Give the extent of all uninfected red blood cells.
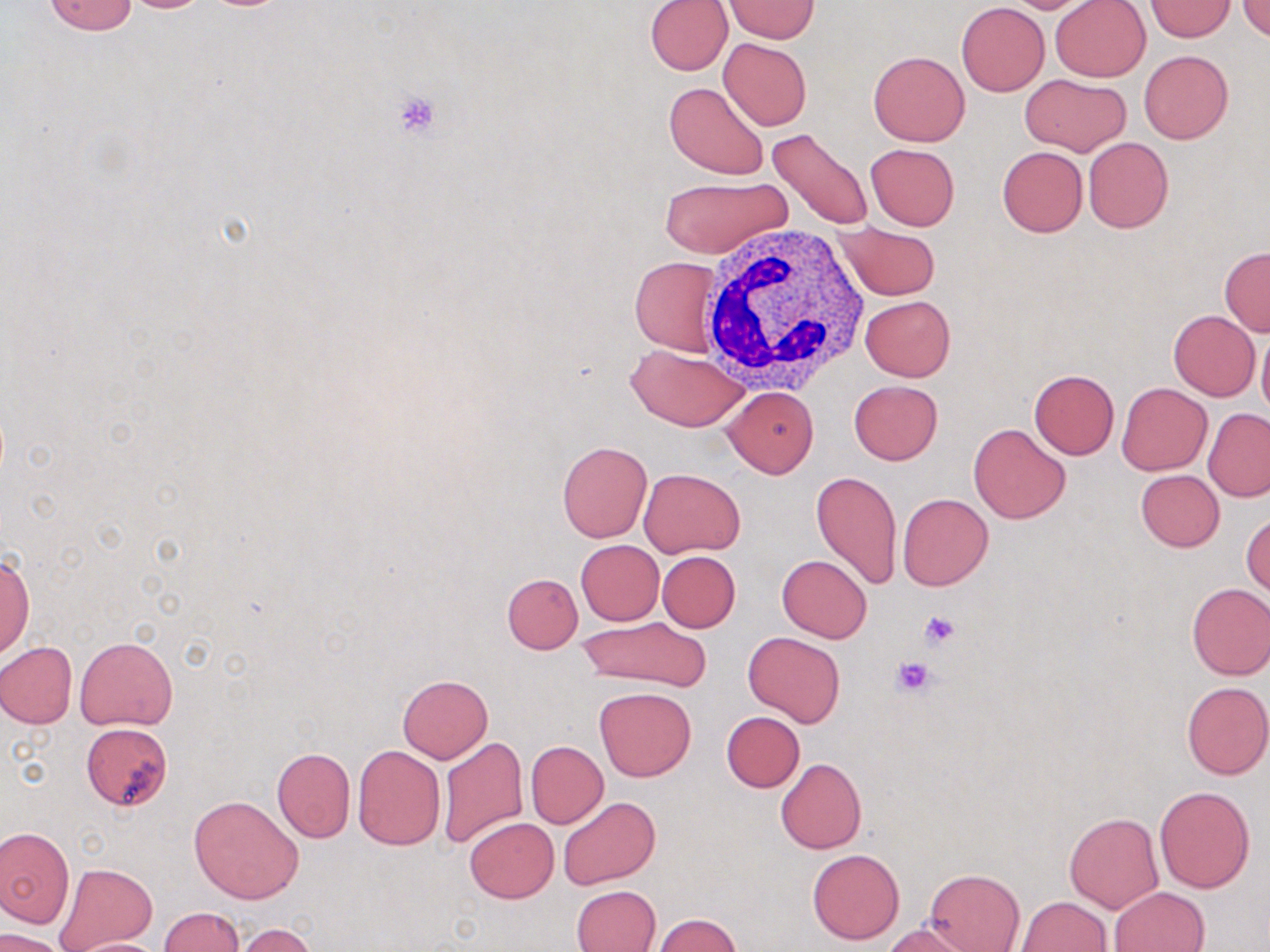

Approximate bounding boxes as [x1, y1, x2, y2] in pixels.
Uninfected red blood cells: [117, 0, 215, 13], [998, 0, 1105, 14], [1049, 0, 1150, 82], [42, 1, 140, 35], [645, 1, 732, 75], [724, 1, 819, 42], [1146, 1, 1237, 41], [1236, 1, 1270, 41], [957, 2, 1049, 96], [719, 38, 811, 130], [867, 50, 970, 146], [1140, 50, 1232, 143], [1019, 75, 1130, 156], [663, 80, 769, 179], [767, 128, 872, 231], [1083, 138, 1174, 233], [865, 143, 960, 230], [996, 146, 1088, 237], [656, 174, 792, 261], [835, 221, 941, 300], [1218, 246, 1270, 336], [629, 256, 722, 356], [860, 295, 955, 381], [1169, 310, 1259, 399], [1256, 325, 1270, 420], [627, 345, 748, 432], [1028, 369, 1120, 459], [849, 380, 943, 464], [1117, 382, 1212, 475], [722, 386, 818, 478], [1203, 408, 1270, 500], [968, 422, 1071, 524], [557, 440, 652, 542], [639, 468, 746, 557], [1135, 469, 1224, 552], [811, 470, 902, 591], [897, 493, 994, 592], [1242, 511, 1269, 598], [576, 540, 664, 625], [656, 551, 740, 632], [1, 552, 33, 658], [776, 555, 872, 643], [502, 572, 583, 653], [1185, 583, 1270, 680], [580, 615, 712, 691], [743, 630, 845, 727], [74, 636, 177, 730], [0, 642, 77, 729], [397, 674, 493, 762], [1181, 681, 1270, 780], [594, 685, 696, 782], [721, 711, 805, 792], [82, 722, 173, 810], [437, 736, 528, 850], [526, 741, 607, 827], [353, 745, 446, 850], [272, 748, 354, 843], [776, 758, 867, 854], [1154, 785, 1255, 892], [188, 795, 303, 904], [558, 796, 660, 890], [1064, 811, 1164, 913], [464, 817, 558, 903], [0, 826, 74, 928], [807, 848, 904, 945], [54, 863, 158, 950], [923, 868, 1025, 952], [571, 884, 660, 952], [1110, 886, 1209, 952], [1017, 897, 1112, 952], [158, 907, 244, 952], [655, 914, 741, 951], [883, 922, 979, 952], [232, 923, 319, 952], [0, 928, 70, 952], [66, 938, 171, 952].

slide-level diagnosis = no evidence of blood parasites
modality = optical microscopy
stain = May-Grünwald-Giemsa
image size = 1270×952 pixels
magnification = 1000x
platelet locations = approximate bounding boxes as [x1, y1, x2, y2] in pixels: [392, 90, 443, 140], [919, 611, 959, 649], [892, 654, 940, 698]
field of view = one of a larger specimen
preparation = thin blood smear
white blood cell locations = approximate bounding boxes as [x1, y1, x2, y2] in pixels: [701, 222, 873, 398]